Describe the morphology of the red blood cells.
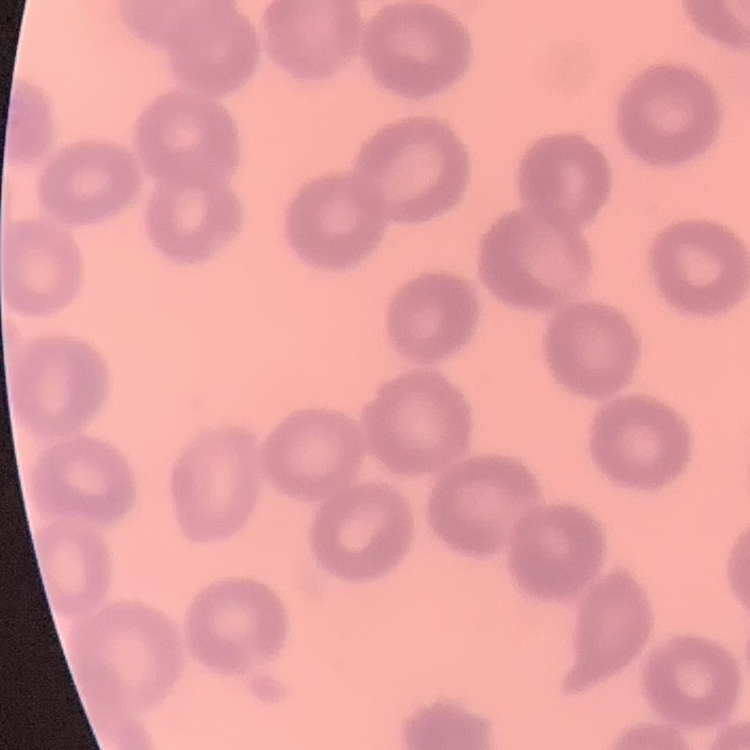
They show no rouleaux formation.

Square crop of a larger photomicrograph. Field's or Giemsa stain. Thin peripheral smear.